Classify this cell by malaria status.
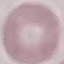

It is uninfected.

Summary:
  - Capture: smartphone camera at the microscope eyepiece
  - Preparation: thin blood film
  - Stain: Giemsa
  - Image type: automatically extracted cell patch, resized to 64 × 64 pixels